Point out each malaria parasite.
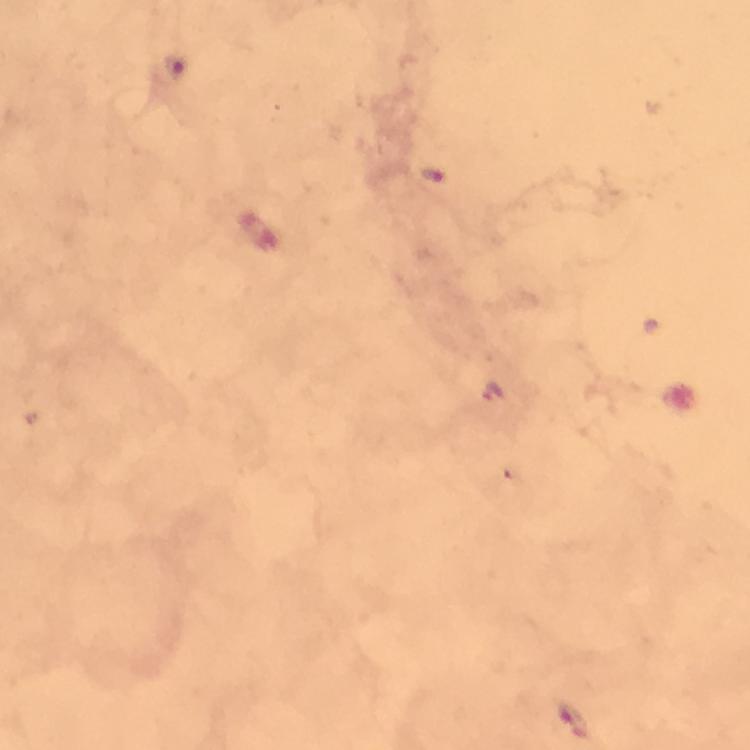

Approximate centers as [x, y] in pixels.
Malaria parasites: [175, 68], [431, 174], [495, 391], [575, 718].

Giemsa stain. Immersion oil applied. Smartphone photograph taken through a microscope. Cropped region of a single field of view. Image is 750×750 pixels. From a malaria diagnostic workup. Thick blood film. 100x magnification.